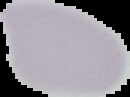

preparation = thin blood smear
image size = 130×97 pixels
image type = cell region segmented out of the field of view; surrounding area masked to black
malaria status = uninfected